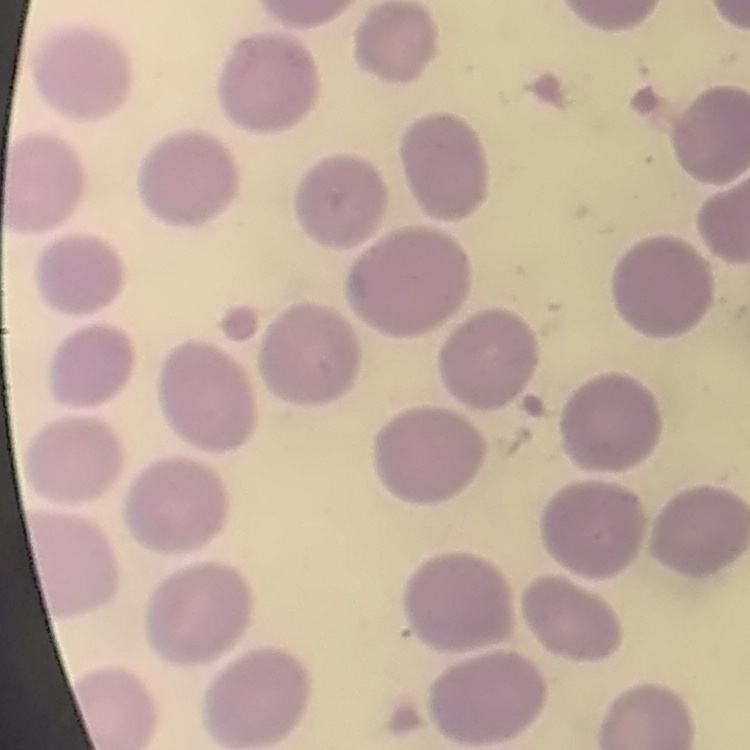
The red blood cells show no rouleaux formation. Field's or Giemsa stain. Thin blood film. Square crop of a larger photomicrograph.